Assess this cell for malaria.
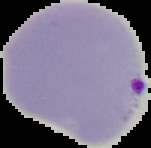

Parasitized.

Summary:
  - Image size: 151×148 pixels
  - Preparation: thin blood smear
  - Image type: cell region segmented out of the field of view; surrounding area masked to black